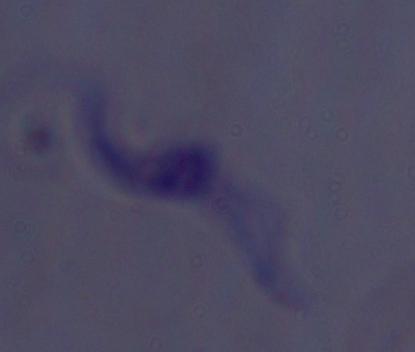

magnification = 1000x
identification = trypanosome
modality = photomicrograph